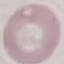
malaria_status: uninfected
preparation: thin smear
stain: Giemsa
image_type: automatically extracted cell patch, resized to 64 × 64 pixels
capture: smartphone through the microscope eyepiece